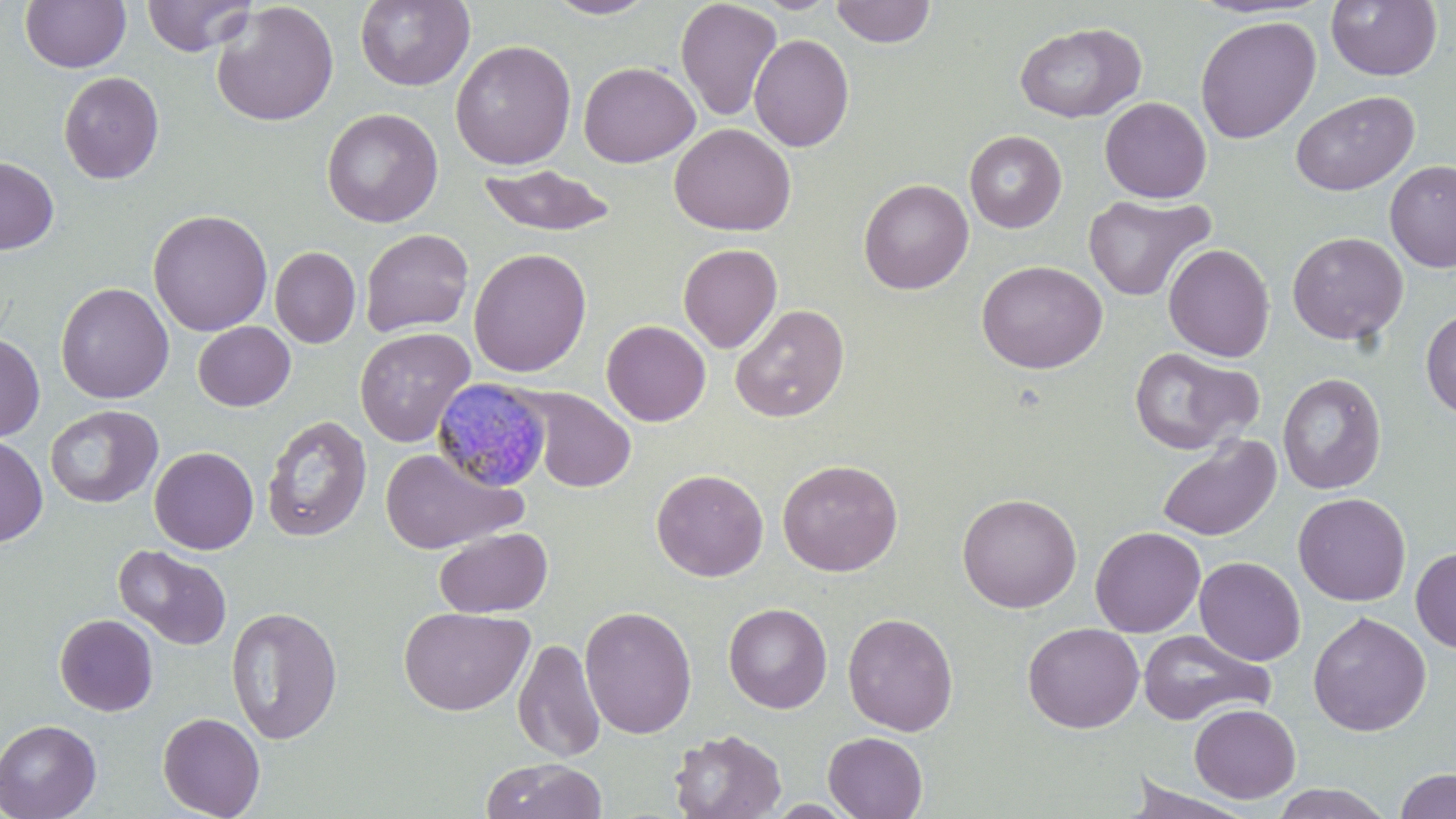

Plasmodium malariae-infected red blood cell locations = approximate bounding boxes as (x1,y1)-(x2,y2) corner pairs in pixels: (431,378)-(553,493)
slide-level diagnosis = Plasmodium malariae
magnification = 1000x
stain = May-Grünwald-Giemsa
image size = 1456×819 pixels
uninfected red blood cell locations = approximate bounding boxes as (x1,y1)-(x2,y2) corner pairs in pixels: (20,0)-(131,73), (141,0)-(257,57), (354,0)-(474,91), (543,0)-(659,19), (675,0)-(783,121), (830,0)-(935,47), (1326,0)-(1442,81), (211,2)-(339,127), (1195,15)-(1321,144), (1014,22)-(1146,123), (749,34)-(854,152), (450,39)-(577,170), (578,61)-(700,167), (58,71)-(164,184), (1290,89)-(1420,197), (1100,96)-(1212,203), (321,107)-(443,228), (669,123)-(796,236), (964,130)-(1067,232), (0,156)-(59,255), (1385,161)-(1456,272), (478,164)-(616,237), (859,178)-(974,294), (1083,193)-(1215,302), (148,209)-(273,336), (360,228)-(474,336), (1287,231)-(1409,345), (678,243)-(782,353), (1163,243)-(1275,361), (269,247)-(361,348), (468,248)-(592,377), (976,260)-(1107,374), (56,282)-(174,403), (730,303)-(849,423), (1421,310)-(1456,420), (601,320)-(711,426), (193,321)-(295,411), (354,326)-(475,448), (0,332)-(45,442), (1128,346)-(1263,456), (1278,372)-(1387,494), (518,387)-(636,492), (44,405)-(162,509), (261,414)-(373,542), (1157,433)-(1281,541), (0,434)-(48,547), (149,446)-(258,554), (380,447)-(526,555), (777,459)-(903,576), (651,468)-(769,581), (956,492)-(1082,613), (1293,492)-(1411,606), (434,526)-(553,618), (1090,526)-(1206,637), (114,544)-(232,650), (1411,546)-(1456,653), (1194,556)-(1305,665), (723,602)-(832,713), (226,605)-(343,745), (579,605)-(698,739), (399,606)-(534,716), (1308,611)-(1431,736), (842,612)-(959,736), (54,614)-(158,717), (1022,623)-(1144,733), (1138,629)-(1274,726), (513,637)-(606,763), (1189,704)-(1300,803), (157,711)-(266,818), (0,719)-(102,819), (669,729)-(786,819), (823,731)-(928,818), (481,758)-(607,819), (1394,767)-(1456,819), (1124,776)-(1258,819), (1270,783)-(1395,818)
modality = light microscopy
preparation = thin blood film
field of view = single